State the preparation type.
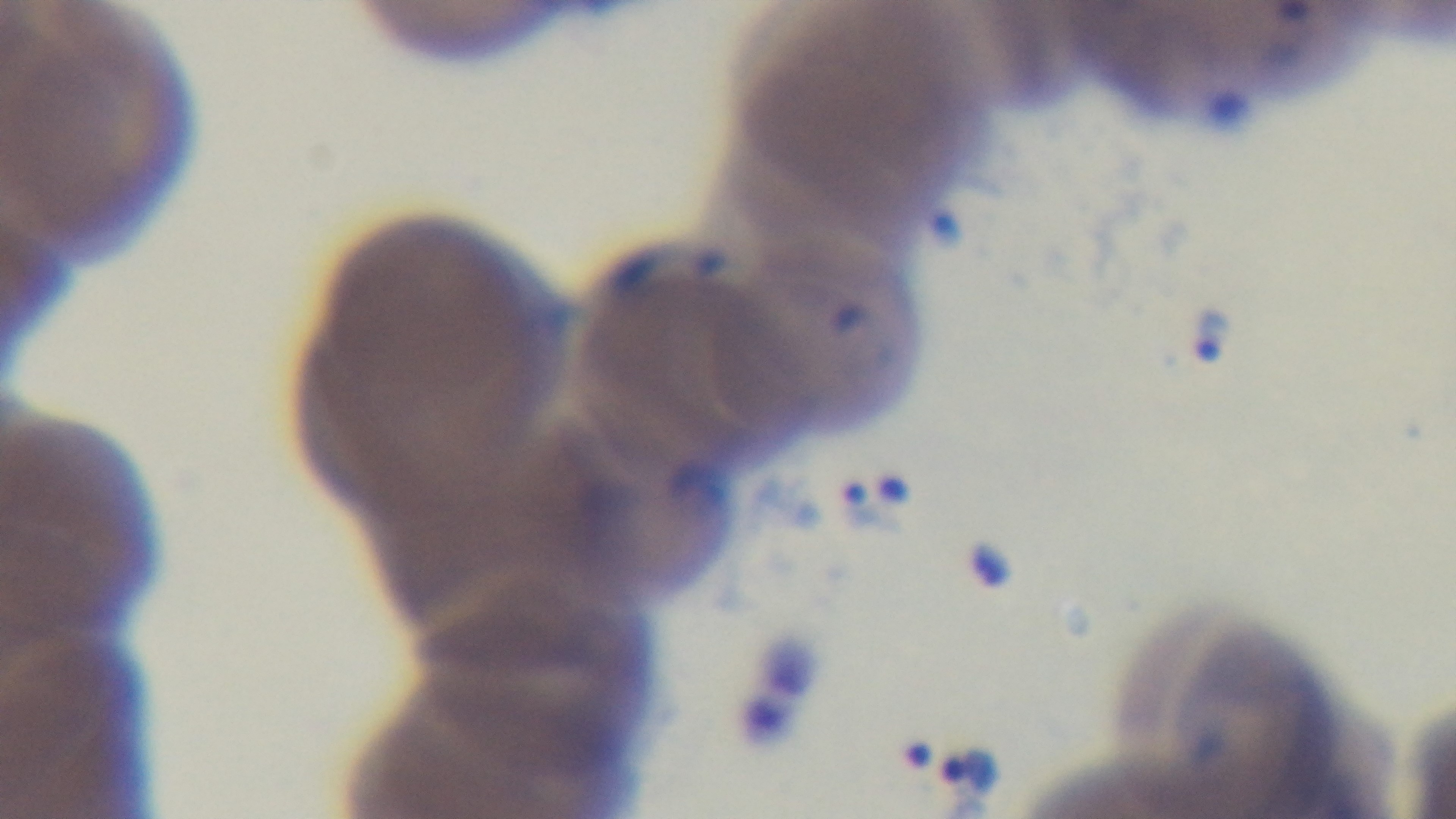
A thin smear.

malaria_status: infected
objective: 100x oil immersion
modality: light microscopy
stain: Giemsa
field_of_view: one from the slide
capture: mounted 4K digital camera